State which cell type is depicted.
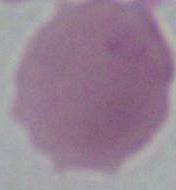

An erythrocyte.

Micrograph. Captured at 1000x magnification.